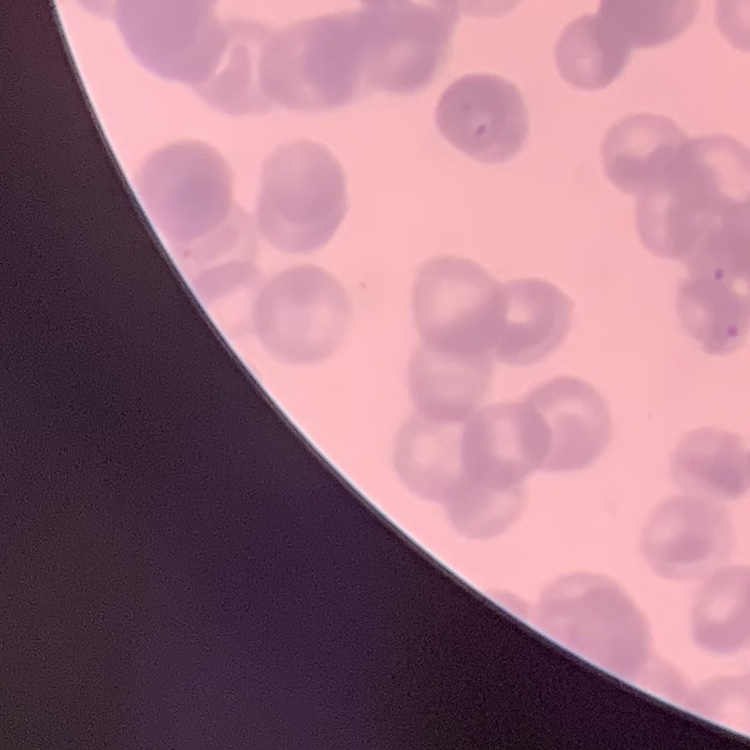
Summary:
  - Red blood cell morphology: rouleaux formation
  - Image type: one tile cut from a larger photomicrograph
  - Stain: Field's or Giemsa
  - Preparation: thin peripheral smear